State which cell type is depicted.
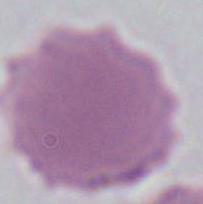
This is an erythrocyte.

modality = micrograph
magnification = 1000x